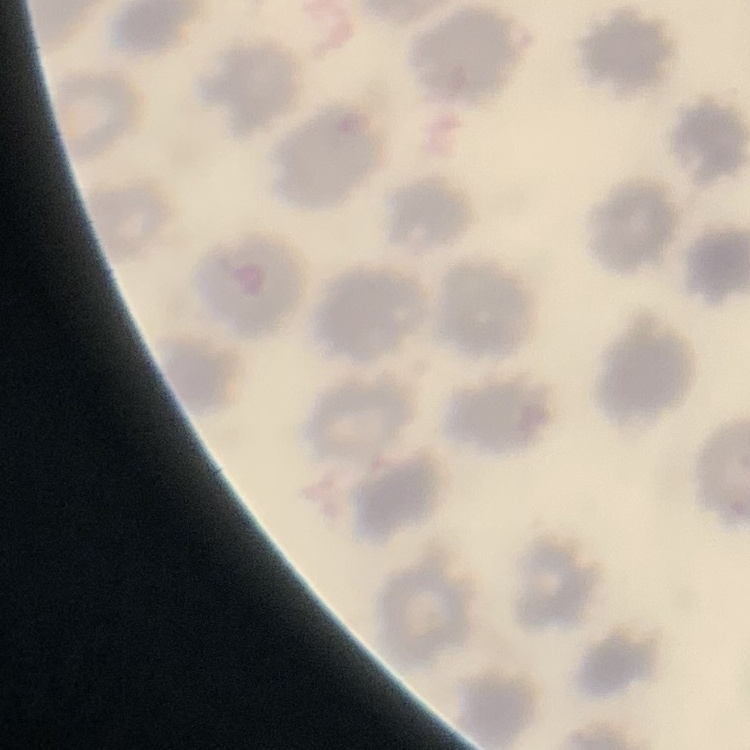

red blood cell morphology = no rouleaux formation
preparation = thin blood smear
image type = square crop of a larger photomicrograph
stain = Field's or Giemsa